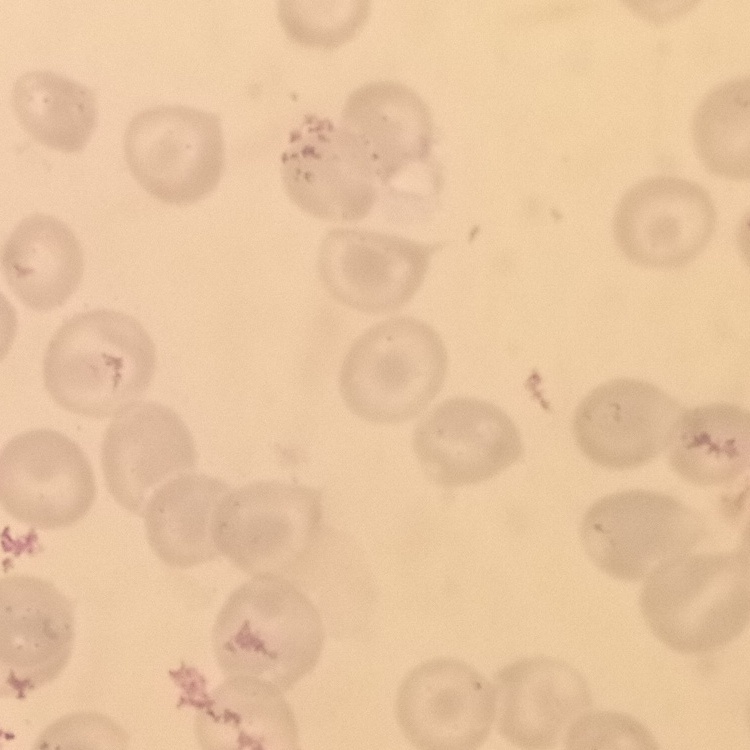
red blood cell morphology = no rouleaux formation
stain = Field's or Giemsa
preparation = thin blood film
image type = one tile cut from a larger photomicrograph